Classify this cell by malaria status.
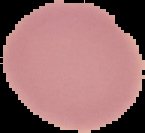

It is uninfected.

Cell region segmented out of the field of view; the surrounding area is masked to black. Image is 145×133 pixels. From a thin blood smear.